State the blood parasite species.
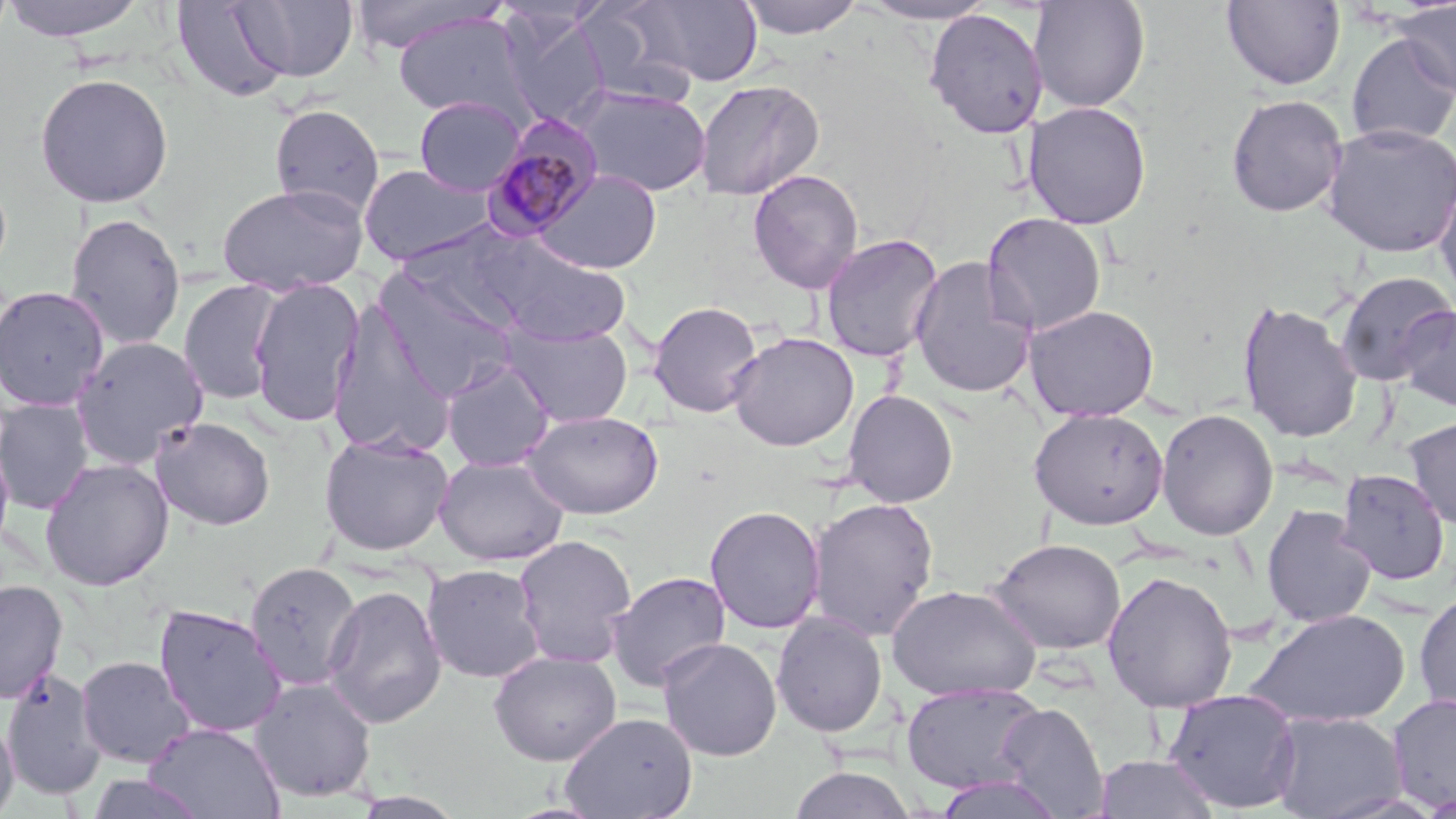

Plasmodium malariae.

stain = May-Grünwald-Giemsa
Plasmodium malariae-infected red blood cell locations = approximate bounding boxes as named x1/y1/x2/y2 corners in pixels: (x1=480, y1=115, x2=603, y2=242)
field of view = one of a larger specimen
modality = optical microscopy
magnification = 1000x
image size = 1456×819 pixels
preparation = thin blood smear
uninfected red blood cell locations = approximate bounding boxes as named x1/y1/x2/y2 corners in pixels: (x1=0, y1=0, x2=152, y2=42), (x1=349, y1=0, x2=508, y2=55), (x1=633, y1=0, x2=763, y2=87), (x1=737, y1=0, x2=864, y2=40), (x1=856, y1=0, x2=1002, y2=25), (x1=1029, y1=0, x2=1150, y2=113), (x1=170, y1=1, x2=295, y2=104), (x1=234, y1=1, x2=358, y2=83), (x1=573, y1=1, x2=700, y2=110), (x1=1221, y1=1, x2=1346, y2=90), (x1=1393, y1=1, x2=1456, y2=99), (x1=498, y1=9, x2=611, y2=130), (x1=924, y1=9, x2=1048, y2=138), (x1=391, y1=12, x2=527, y2=120), (x1=1345, y1=33, x2=1456, y2=149), (x1=35, y1=72, x2=174, y2=208), (x1=695, y1=79, x2=824, y2=200), (x1=572, y1=85, x2=712, y2=197), (x1=1225, y1=94, x2=1348, y2=217), (x1=414, y1=96, x2=526, y2=196), (x1=1022, y1=100, x2=1152, y2=229), (x1=269, y1=104, x2=384, y2=219), (x1=1321, y1=122, x2=1456, y2=258), (x1=358, y1=162, x2=495, y2=266), (x1=533, y1=168, x2=662, y2=275), (x1=747, y1=169, x2=864, y2=294), (x1=1434, y1=170, x2=1456, y2=301), (x1=216, y1=182, x2=369, y2=296), (x1=65, y1=211, x2=186, y2=349), (x1=982, y1=212, x2=1107, y2=335), (x1=820, y1=233, x2=944, y2=363), (x1=482, y1=237, x2=631, y2=346), (x1=909, y1=257, x2=1038, y2=399), (x1=372, y1=266, x2=521, y2=399), (x1=1334, y1=271, x2=1454, y2=386), (x1=249, y1=277, x2=363, y2=428), (x1=178, y1=279, x2=285, y2=406), (x1=0, y1=285, x2=111, y2=412), (x1=327, y1=299, x2=456, y2=458), (x1=1237, y1=300, x2=1363, y2=443), (x1=648, y1=301, x2=763, y2=418), (x1=1023, y1=304, x2=1160, y2=421), (x1=1396, y1=305, x2=1456, y2=413), (x1=502, y1=322, x2=633, y2=427), (x1=728, y1=332, x2=858, y2=451), (x1=70, y1=336, x2=209, y2=468), (x1=441, y1=360, x2=555, y2=472), (x1=842, y1=389, x2=959, y2=508), (x1=0, y1=398, x2=95, y2=515), (x1=1028, y1=407, x2=1169, y2=530), (x1=1156, y1=408, x2=1279, y2=541), (x1=523, y1=409, x2=665, y2=519), (x1=1404, y1=415, x2=1456, y2=530), (x1=150, y1=416, x2=276, y2=530), (x1=318, y1=432, x2=454, y2=556), (x1=0, y1=433, x2=15, y2=562), (x1=434, y1=454, x2=569, y2=565), (x1=39, y1=457, x2=174, y2=591), (x1=1337, y1=468, x2=1451, y2=587), (x1=807, y1=497, x2=940, y2=641), (x1=1261, y1=504, x2=1377, y2=628), (x1=704, y1=505, x2=826, y2=635), (x1=512, y1=534, x2=637, y2=669), (x1=987, y1=537, x2=1127, y2=655), (x1=245, y1=561, x2=363, y2=692), (x1=422, y1=563, x2=547, y2=683), (x1=606, y1=570, x2=731, y2=692), (x1=1101, y1=570, x2=1238, y2=713), (x1=0, y1=579, x2=68, y2=704), (x1=323, y1=584, x2=447, y2=728), (x1=886, y1=584, x2=1042, y2=702), (x1=1414, y1=590, x2=1456, y2=718), (x1=154, y1=603, x2=287, y2=737), (x1=1246, y1=608, x2=1412, y2=728), (x1=771, y1=612, x2=888, y2=737), (x1=658, y1=638, x2=782, y2=761), (x1=489, y1=650, x2=622, y2=765), (x1=75, y1=655, x2=195, y2=768), (x1=2, y1=667, x2=106, y2=798), (x1=248, y1=677, x2=377, y2=803), (x1=901, y1=682, x2=1046, y2=795), (x1=1163, y1=688, x2=1302, y2=813), (x1=1386, y1=693, x2=1456, y2=812), (x1=995, y1=702, x2=1110, y2=817), (x1=1268, y1=711, x2=1408, y2=819), (x1=559, y1=712, x2=698, y2=819), (x1=0, y1=715, x2=18, y2=817), (x1=143, y1=721, x2=285, y2=819), (x1=1093, y1=753, x2=1221, y2=818), (x1=788, y1=765, x2=917, y2=819), (x1=932, y1=772, x2=1067, y2=818), (x1=86, y1=773, x2=208, y2=818)